Identify the blood parasite species.
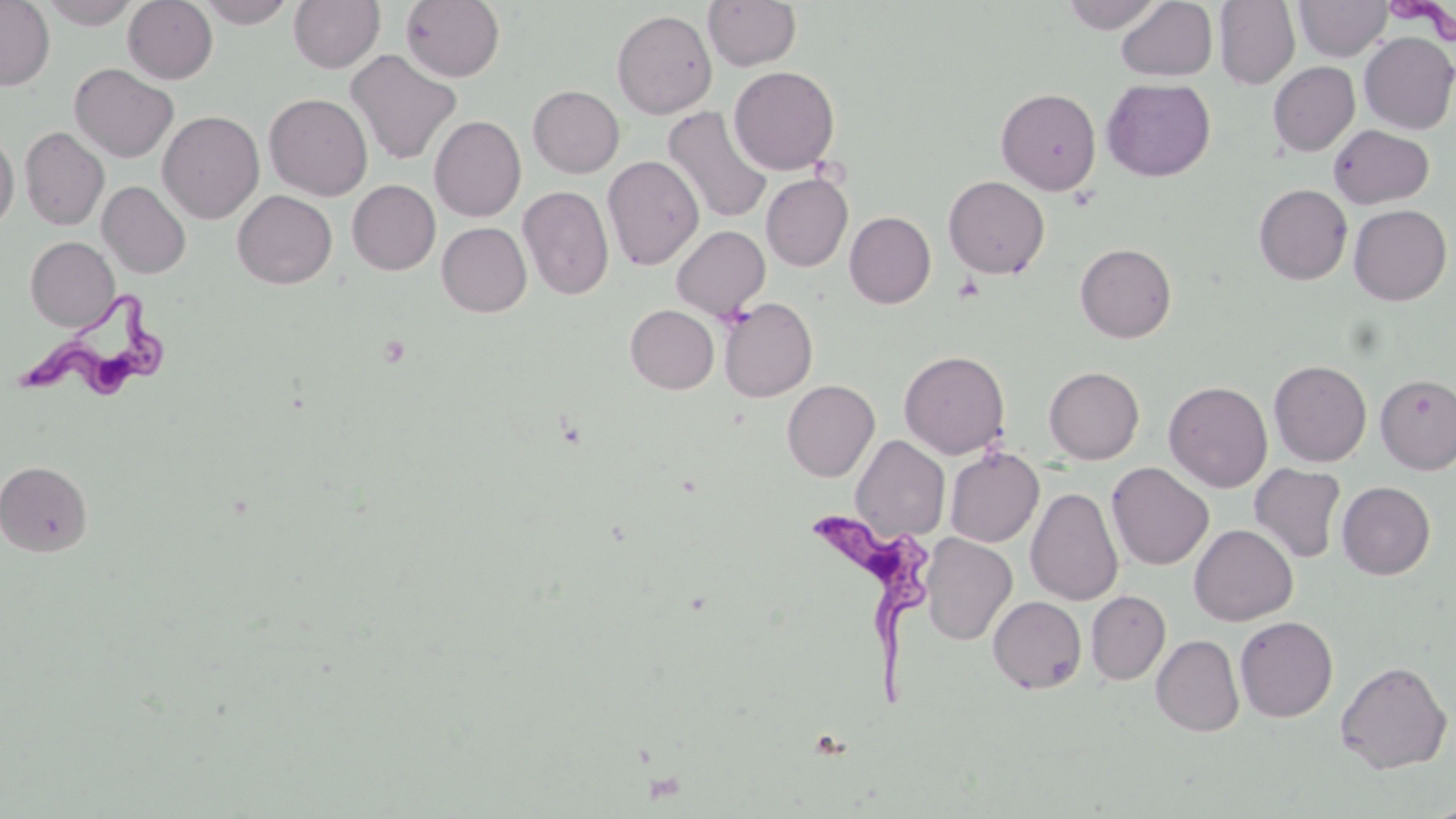

Trypanosoma brucei.

Approximate bounding boxes as [x1, y1, x2, y2] in pixels. Trypanosoma brucei locations: [5, 293, 169, 408], [804, 499, 930, 704]. Uninfected red blood cell locations: [0, 0, 55, 90], [39, 0, 141, 29], [123, 0, 218, 84], [195, 0, 296, 28], [289, 0, 385, 73], [401, 0, 504, 81], [703, 0, 802, 71], [1061, 0, 1164, 33], [1214, 0, 1300, 90], [1294, 0, 1392, 61], [1116, 1, 1218, 82], [612, 9, 717, 119], [1358, 32, 1456, 134], [346, 49, 462, 166], [1268, 62, 1360, 156], [69, 63, 178, 162], [728, 65, 840, 175], [1102, 78, 1216, 182], [528, 85, 624, 177], [997, 87, 1101, 195], [264, 94, 372, 200], [662, 106, 773, 224], [158, 110, 264, 223], [429, 115, 526, 221], [1328, 124, 1435, 208], [20, 126, 109, 230], [0, 133, 18, 231], [603, 155, 704, 271], [761, 173, 853, 271], [943, 175, 1050, 279], [347, 180, 440, 275], [97, 181, 191, 279], [1254, 184, 1352, 285], [518, 186, 614, 300], [232, 190, 337, 289], [1349, 204, 1452, 305], [845, 211, 936, 309], [437, 222, 532, 317], [671, 225, 770, 320], [25, 237, 119, 331], [1075, 243, 1177, 343], [718, 297, 817, 402], [625, 305, 719, 394], [899, 350, 1010, 459], [1268, 360, 1372, 467], [1044, 366, 1144, 463], [1375, 372, 1456, 474], [782, 380, 879, 481], [1164, 381, 1272, 492], [850, 435, 950, 542], [945, 447, 1044, 547], [0, 461, 93, 557], [1107, 462, 1214, 570], [1249, 464, 1347, 563], [1337, 481, 1435, 579], [1026, 487, 1123, 606], [1189, 524, 1298, 625], [921, 533, 1017, 645], [1086, 590, 1170, 684], [988, 596, 1087, 694], [1234, 615, 1338, 722], [1151, 635, 1244, 736], [1335, 660, 1452, 774]. One field of a larger specimen. 1000x magnification. Image is 1456×819 pixels. Light microscopy. Thin blood smear. May-Grünwald-Giemsa-stained preparation.